Locate every malaria parasite.
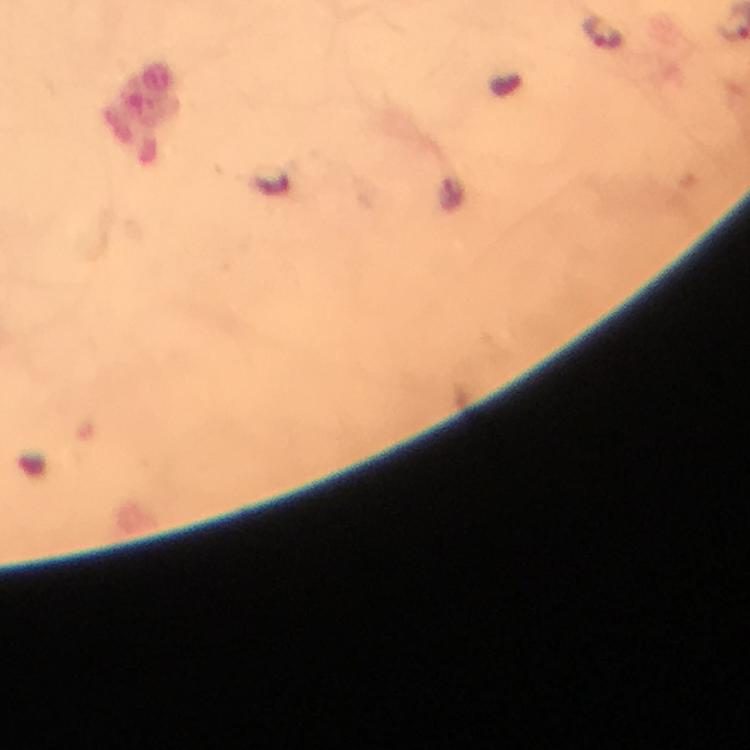

Approximate object centers, in pixels from the top-left corner.
Malaria parasites: (x=603, y=33).

Summary:
  - Context: from a malaria diagnostic workup
  - Stain: Giemsa
  - Magnification: 100x
  - Preparation: thick blood film
  - Immersion oil: applied
  - Capture: smartphone photograph through a microscope
  - Cropped from: one field of view
  - Image size: 750×750 pixels